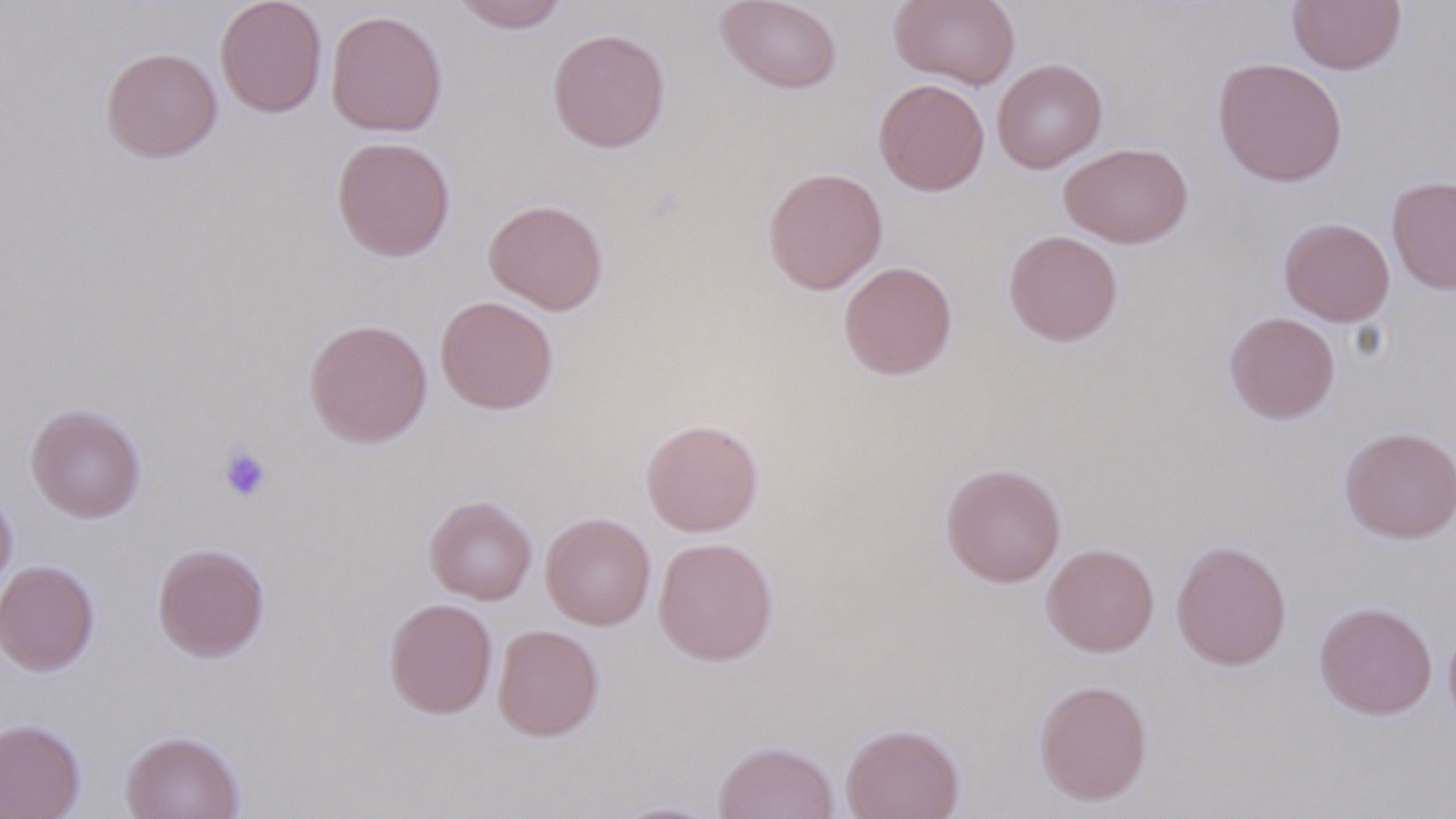
slide-level diagnosis = negative for blood parasites
image size = 1456×819 pixels
magnification = 1000x
preparation = thin blood smear
platelet locations = approximate bounding boxes as (x1, y1, x2, y2) in pixels: (218, 445, 272, 502)
modality = light microscopy
field of view = single
uninfected red blood cell locations = approximate bounding boxes as (x1, y1, x2, y2) in pixels: (215, 0, 327, 117), (716, 0, 842, 94), (888, 0, 1020, 89), (450, 1, 570, 33), (1287, 1, 1406, 74), (325, 10, 448, 137), (547, 28, 670, 153), (100, 46, 222, 163), (1213, 57, 1347, 187), (992, 58, 1107, 173), (873, 78, 990, 196), (331, 136, 456, 262), (1060, 143, 1192, 248), (762, 167, 888, 294), (1387, 175, 1456, 294), (483, 199, 609, 315), (1279, 218, 1394, 326), (1004, 230, 1122, 346), (838, 261, 958, 380), (435, 296, 559, 414), (1224, 312, 1339, 424), (303, 318, 433, 448), (25, 403, 147, 523), (640, 418, 764, 536), (1339, 427, 1456, 543), (941, 463, 1066, 587), (0, 485, 17, 601), (425, 495, 537, 604), (540, 512, 655, 630), (653, 536, 779, 666), (1170, 539, 1291, 671), (152, 542, 270, 662), (1041, 543, 1158, 657), (0, 559, 100, 676), (384, 597, 497, 718), (1314, 602, 1437, 719), (492, 624, 604, 742), (1034, 679, 1153, 805), (0, 718, 86, 819), (841, 722, 965, 819), (121, 730, 244, 818), (713, 740, 840, 819), (608, 800, 723, 818)
stain = May-Grünwald-Giemsa